Report the malaria status of this cell.
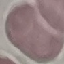

It is uninfected.

Giemsa-stained preparation. Acquired by smartphone through the microscope eyepiece. Cell patch, automatically extracted from a larger field of view and resized to 64 × 64 pixels. Thin blood film.